Name the parasite shown.
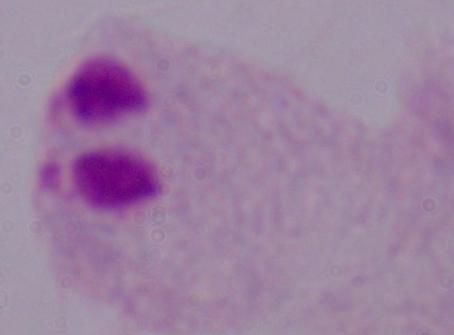
This is a trichomonad.

modality: micrograph
magnification: 1000x